Assess this cell for malaria.
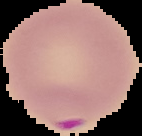
It is parasitized.

Summary:
  - Image type: segmented cell region with the area outside set to black
  - Image size: 142×136 pixels
  - Preparation: thin blood smear